Describe the morphology of the erythrocytes.
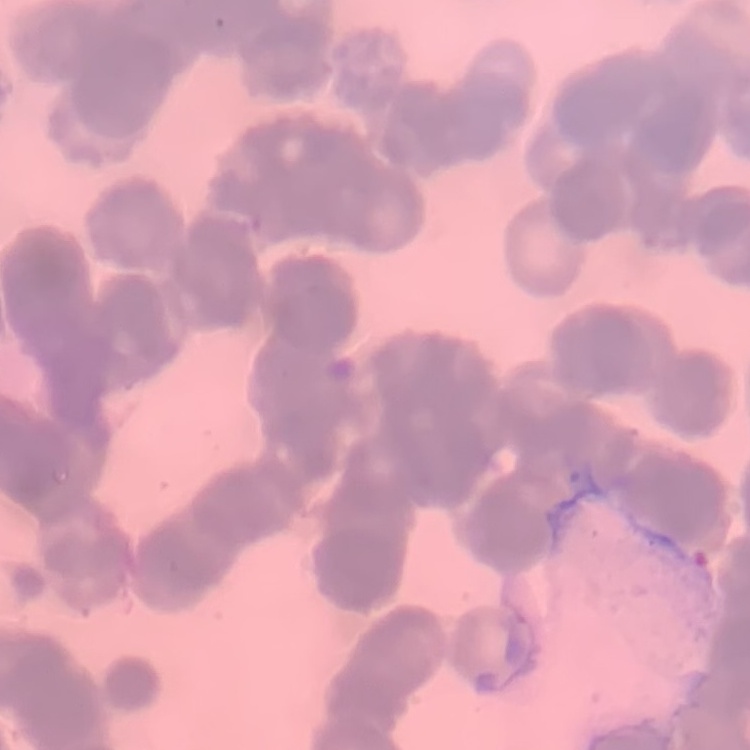

Rouleaux formation.

image_type: square crop of a larger photomicrograph
stain: Field's or Giemsa
preparation: thin blood smear